Comment on the morphology of the erythrocytes.
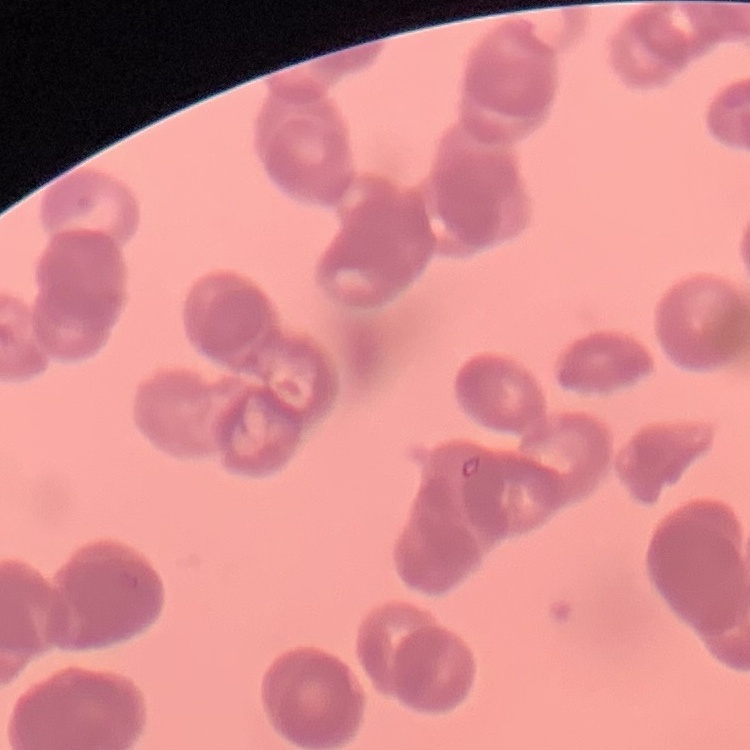

Rouleaux formation.

Field's or Giemsa stain. Square crop of a larger photomicrograph. Thin peripheral smear.